Identify the blood parasite species.
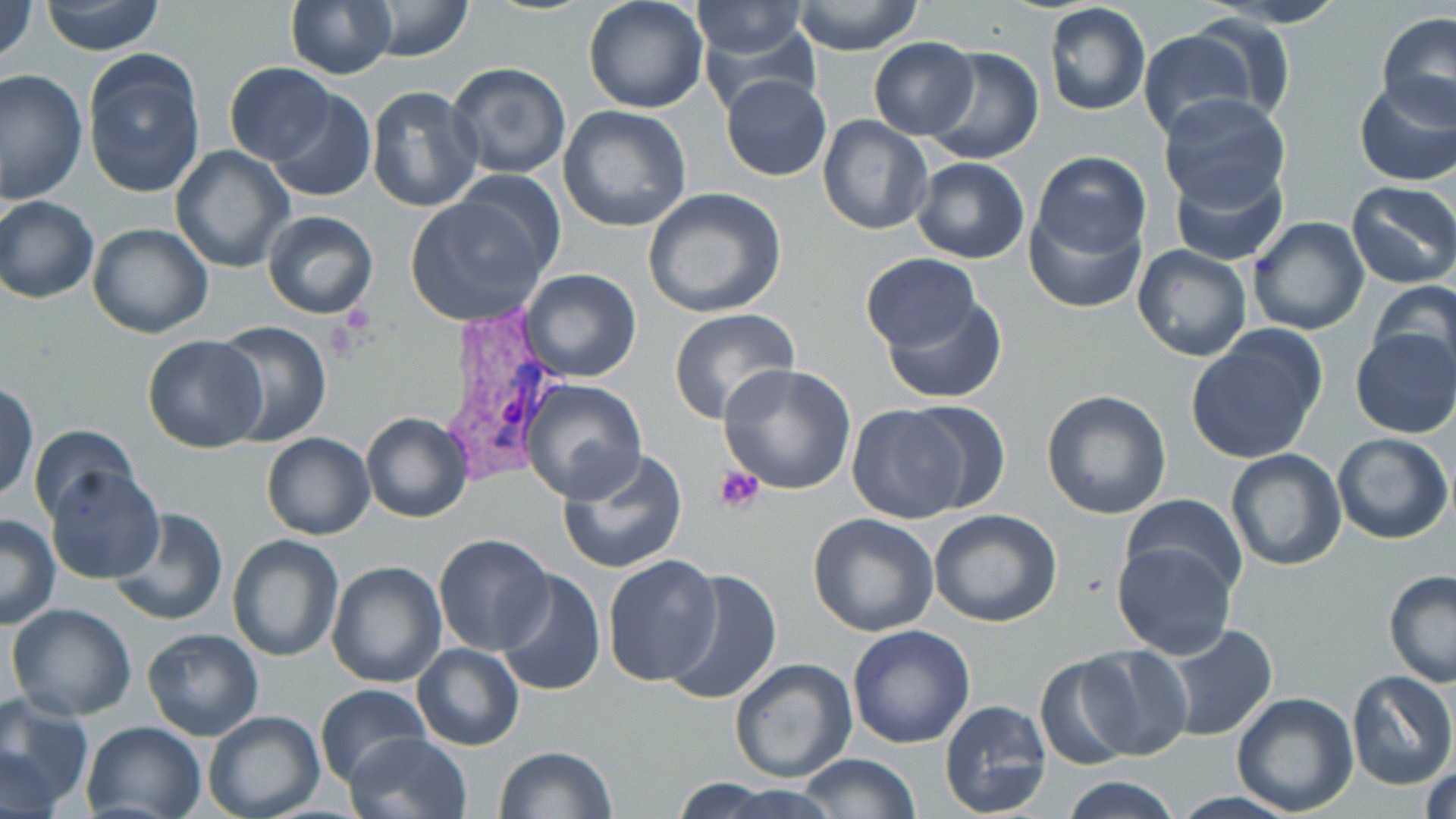

Plasmodium vivax.

{
  "field_of_view": "one of a larger specimen",
  "image_size": "1456×819 pixels",
  "magnification": "1000x",
  "platelet_locations": "approximate bounding boxes as [x1, y1, x2, y2] in pixels: [714, 465, 765, 515]",
  "plasmodium_vivax_infected_red_blood_cell_locations": "approximate bounding boxes as [x1, y1, x2, y2] in pixels: [433, 313, 565, 491]",
  "modality": "light microscopy",
  "uninfected_red_blood_cell_locations": "approximate bounding boxes as [x1, y1, x2, y2] in pixels: [0, 0, 38, 66], [40, 0, 165, 57], [358, 0, 473, 60], [1203, 0, 1351, 28], [285, 1, 396, 78], [583, 1, 710, 114], [691, 2, 810, 61], [791, 2, 925, 55], [1045, 2, 1151, 116], [696, 12, 821, 114], [1376, 12, 1456, 125], [1174, 16, 1293, 121], [1137, 29, 1260, 142], [868, 37, 978, 139], [922, 46, 1044, 166], [83, 52, 205, 199], [225, 62, 336, 165], [444, 62, 573, 181], [0, 68, 88, 206], [721, 74, 832, 182], [1353, 76, 1455, 186], [365, 86, 483, 212], [266, 89, 377, 203], [1157, 93, 1291, 210], [557, 105, 692, 231], [818, 115, 932, 235], [170, 146, 293, 272], [1031, 151, 1152, 259], [911, 156, 1031, 265], [1171, 161, 1289, 265], [1347, 181, 1456, 289], [642, 187, 788, 318], [406, 190, 555, 326], [1, 197, 99, 304], [1023, 202, 1147, 316], [263, 211, 379, 321], [1246, 217, 1369, 336], [87, 222, 213, 337], [1133, 244, 1253, 363], [861, 254, 978, 351], [516, 269, 642, 383], [1367, 279, 1456, 384], [880, 294, 1008, 404], [667, 308, 800, 426], [209, 319, 331, 446], [1349, 329, 1456, 440], [1184, 330, 1326, 464], [140, 335, 268, 454], [718, 363, 857, 495], [520, 379, 647, 502], [1, 380, 37, 502], [1040, 390, 1171, 520], [896, 398, 1014, 513], [847, 404, 970, 524], [362, 412, 473, 523], [28, 424, 140, 525], [1331, 431, 1454, 544], [262, 432, 376, 540], [556, 447, 688, 575], [1224, 450, 1347, 572], [45, 466, 165, 584], [1123, 493, 1246, 600], [108, 509, 229, 627], [928, 509, 1061, 627], [0, 513, 60, 628], [807, 513, 939, 636], [433, 533, 554, 655], [227, 535, 344, 662], [1110, 540, 1237, 660], [603, 554, 724, 687], [327, 560, 448, 688], [494, 568, 605, 697], [659, 568, 784, 707], [1383, 572, 1456, 686], [6, 601, 138, 721], [847, 624, 976, 749], [1157, 624, 1279, 744], [143, 628, 263, 741], [411, 643, 524, 750], [1076, 644, 1193, 761], [1033, 654, 1145, 770], [729, 658, 858, 785], [1345, 670, 1455, 790], [314, 683, 429, 787], [1230, 690, 1360, 816], [0, 697, 93, 811], [938, 700, 1053, 818], [203, 708, 325, 819], [79, 720, 206, 819], [346, 732, 473, 819], [0, 745, 64, 819], [493, 745, 617, 819], [798, 752, 922, 819], [1420, 761, 1456, 819], [1059, 774, 1183, 818], [664, 780, 832, 819]",
  "preparation": "thin blood film",
  "stain": "May-Grünwald-Giemsa"
}